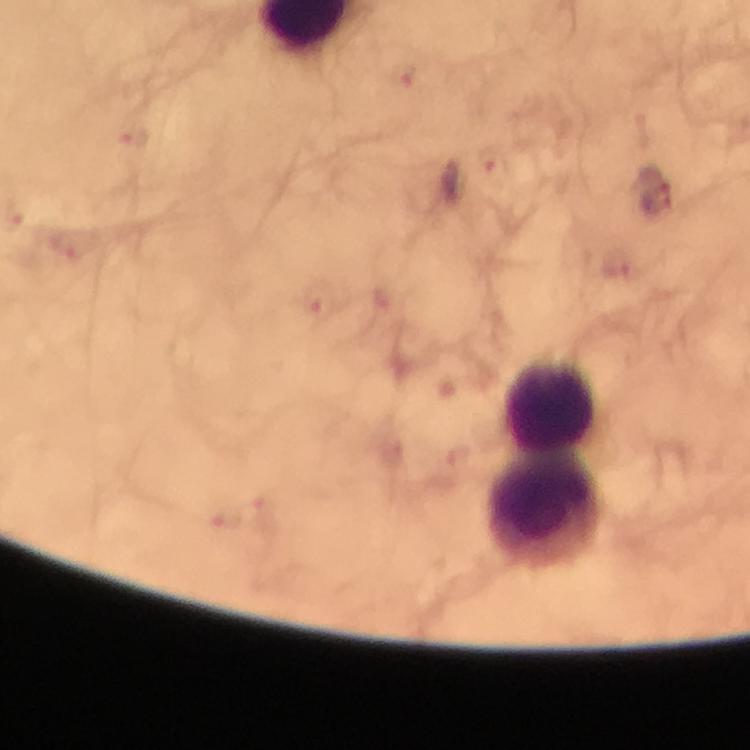
preparation: thick blood smear
malaria_parasite_locations: 'approximate centers as [x, y] in pixels: [403, 75], [132, 134], [495, 162], [657, 200], [64, 245], [616, 266], [315, 303], [394, 450], [460, 453], [261, 509], [223, 519]'
immersion_oil: applied
capture: smartphone photograph through a microscope
stain: Giemsa
leukocyte_locations: 'approximate centers as [x, y] in pixels: [549, 405], [546, 512]'
cropped_from: a single field of view
magnification: 100x
image_size: 750×750 pixels
context: from a malaria diagnostic workup